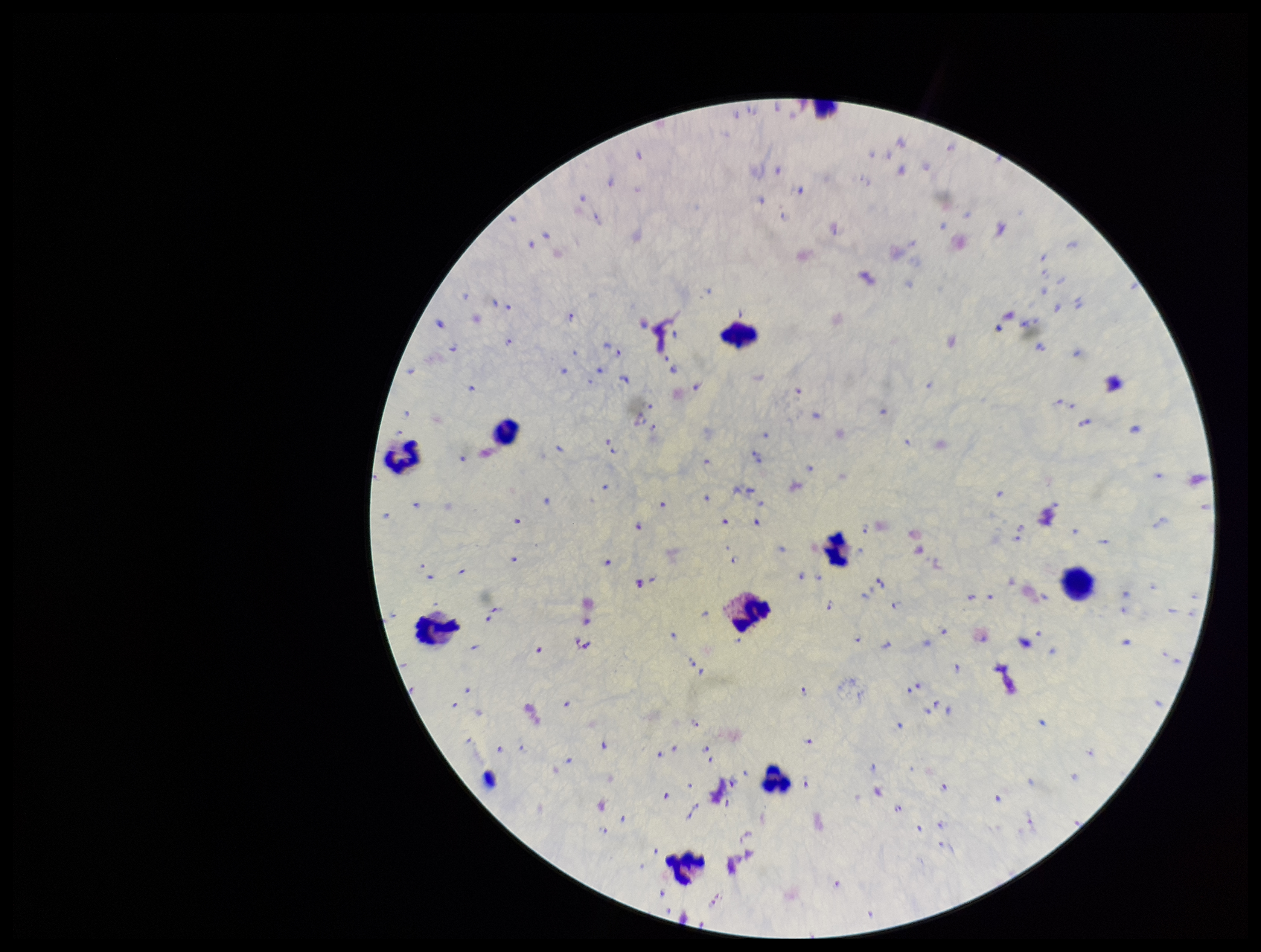

Summary:
  - Species reported for this patient: Plasmodium falciparum
  - Stain: Giemsa
  - Image size: 1261×952 pixels
  - Patient malaria status: positive
  - Leukocyte count: 9
  - Field of view: one from this slide
  - Parasite count: 199
  - Preparation: thick
  - Capture: smartphone photograph through the microscope eyepiece
  - Plasmodium parasites: seen